Give the position of every Plasmodium parasite visible.
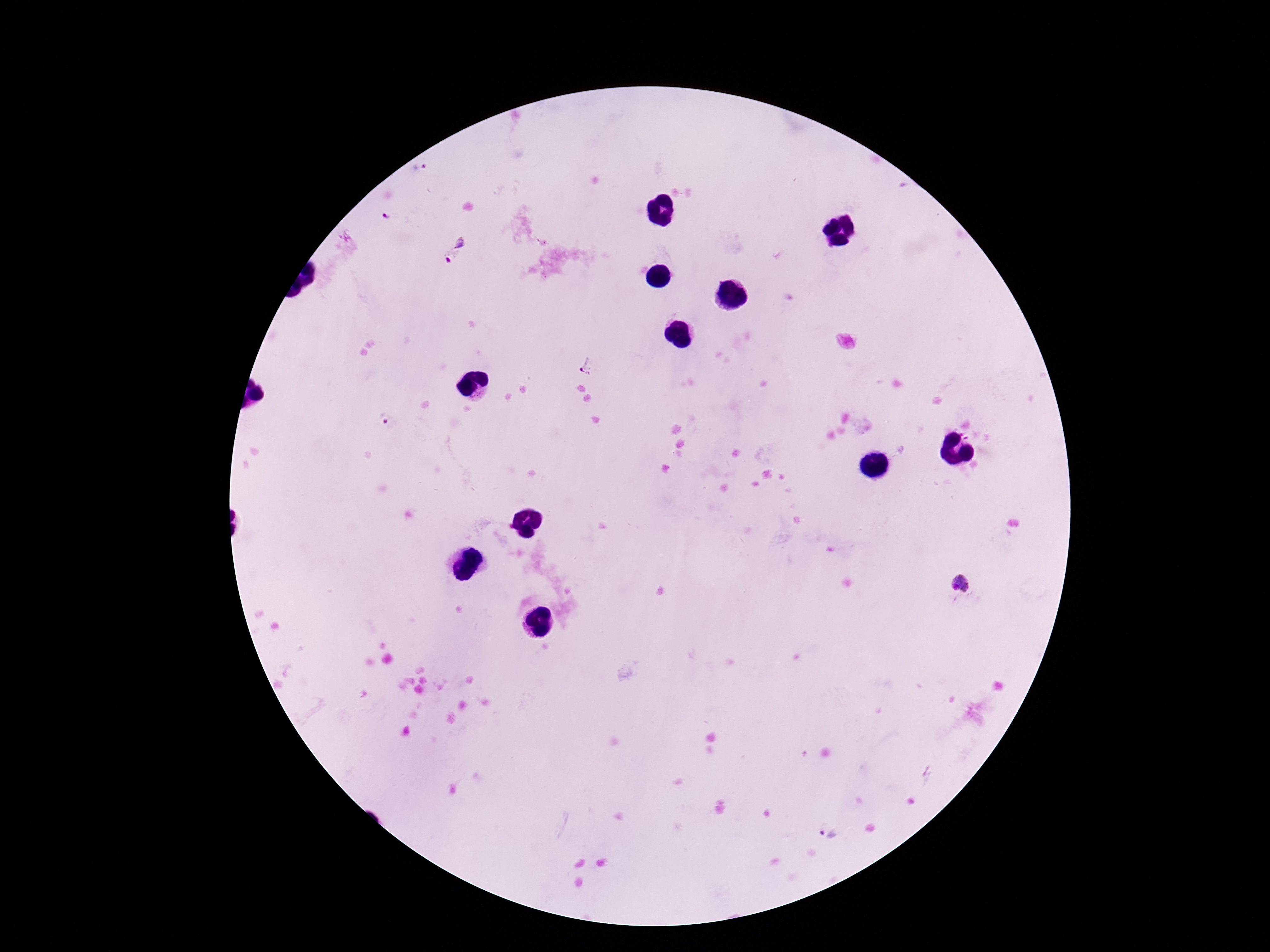

Approximate object centers, in pixels from the top-left corner.
Plasmodium parasites: (x=420, y=172), (x=386, y=218), (x=456, y=249), (x=588, y=367), (x=382, y=421), (x=963, y=584), (x=827, y=834).

Image is 1270×952 pixels. Thick blood smear. Single field of view. Giemsa-stained preparation. Patient malaria status: infected. Photographed through the microscope eyepiece with a smartphone camera. 100x magnification.